Assess the morphology of the red blood cells.
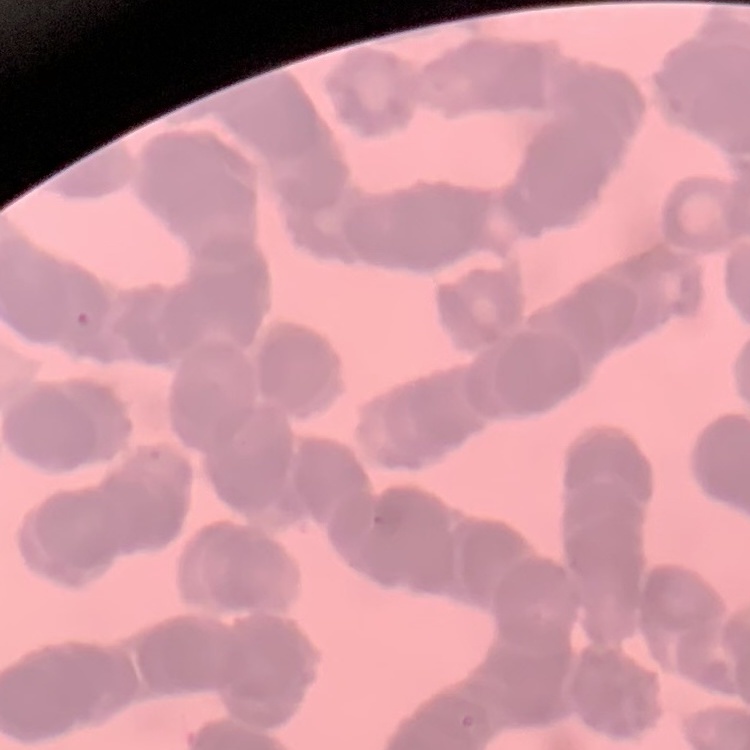
They show rouleaux formation.

stain = Field's or Giemsa
image type = square crop of a larger photomicrograph
preparation = thin peripheral smear